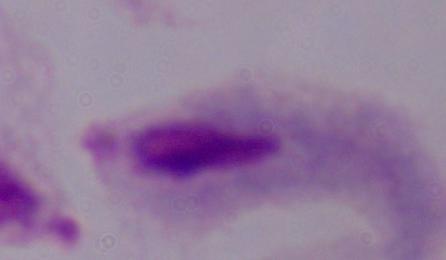
A trichomonad is seen. Captured at 1000x magnification. Photomicrograph.